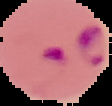

Summary:
  - Malaria status: parasitized
  - Image type: segmented cell region with the area outside set to black
  - Preparation: thin blood smear
  - Image size: 112×106 pixels